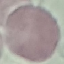

Malaria status: uninfected. Photographed with a smartphone camera at the microscope eyepiece. Cell patch, automatically extracted from a larger field of view and resized to 64 × 64 pixels. Giemsa stain. Thin smear of blood.